Mark where platelets are.
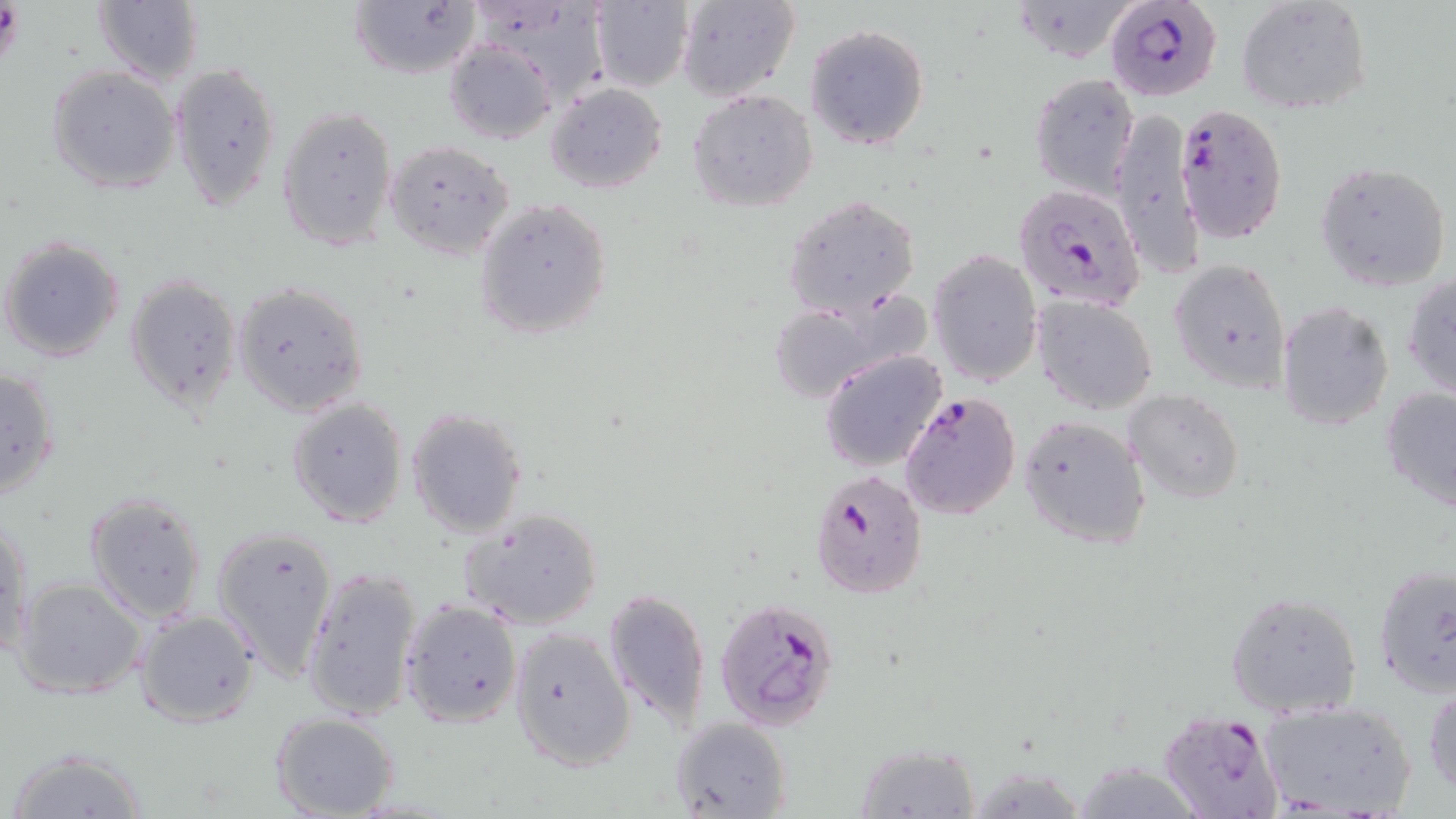

Approximate bounding boxes as (x1, y1, x2, y2) in pixels.
Platelets: (0, 4, 26, 67).

Summary:
  - Uninfected red blood cell locations: (588, 0, 693, 91), (674, 0, 800, 103), (1006, 0, 1143, 64), (1234, 0, 1373, 116), (92, 1, 204, 87), (348, 2, 481, 80), (804, 24, 929, 151), (442, 38, 558, 145), (170, 61, 282, 211), (47, 65, 182, 194), (1029, 70, 1140, 198), (545, 82, 668, 193), (688, 90, 818, 212), (277, 105, 399, 251), (1110, 112, 1204, 276), (384, 140, 515, 261), (1316, 161, 1450, 291), (784, 195, 920, 318), (474, 199, 611, 339), (1, 236, 127, 363), (927, 248, 1044, 387), (1167, 256, 1291, 394), (125, 273, 242, 414), (1403, 275, 1456, 405), (231, 281, 369, 418), (1032, 295, 1159, 415), (763, 297, 916, 406), (1276, 302, 1394, 431), (820, 349, 949, 471), (1, 366, 61, 499), (1380, 388, 1456, 513), (1123, 389, 1246, 503), (288, 397, 409, 528), (405, 407, 527, 538), (1017, 415, 1150, 549), (83, 491, 209, 622), (462, 508, 602, 630), (1, 515, 33, 658), (210, 522, 340, 681), (302, 563, 424, 723), (1374, 563, 1456, 700), (13, 576, 148, 700), (602, 588, 711, 728), (1225, 590, 1363, 717), (399, 598, 522, 728), (134, 608, 260, 727), (508, 627, 634, 772), (1426, 683, 1456, 799), (1259, 700, 1416, 819), (270, 713, 400, 819), (669, 717, 792, 819), (855, 741, 980, 817), (4, 746, 150, 819), (1071, 760, 1205, 817), (964, 762, 1092, 819)
  - Plasmodium falciparum-infected red blood cell locations: (1105, 0, 1224, 103), (1174, 104, 1289, 245), (1012, 182, 1145, 318), (900, 389, 1021, 520), (809, 469, 928, 599), (714, 596, 841, 730), (1159, 710, 1285, 819)
  - Slide-level diagnosis: Plasmodium falciparum
  - Preparation: thin blood smear
  - Modality: optical microscopy
  - Image size: 1456×819 pixels
  - Magnification: 1000x
  - Field of view: one of a larger specimen
  - Stain: May-Grünwald-Giemsa